State which parasite is depicted.
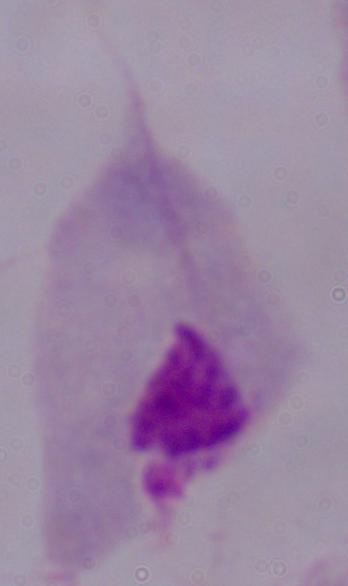
A trichomonad.

magnification = 1000x
modality = photomicrograph